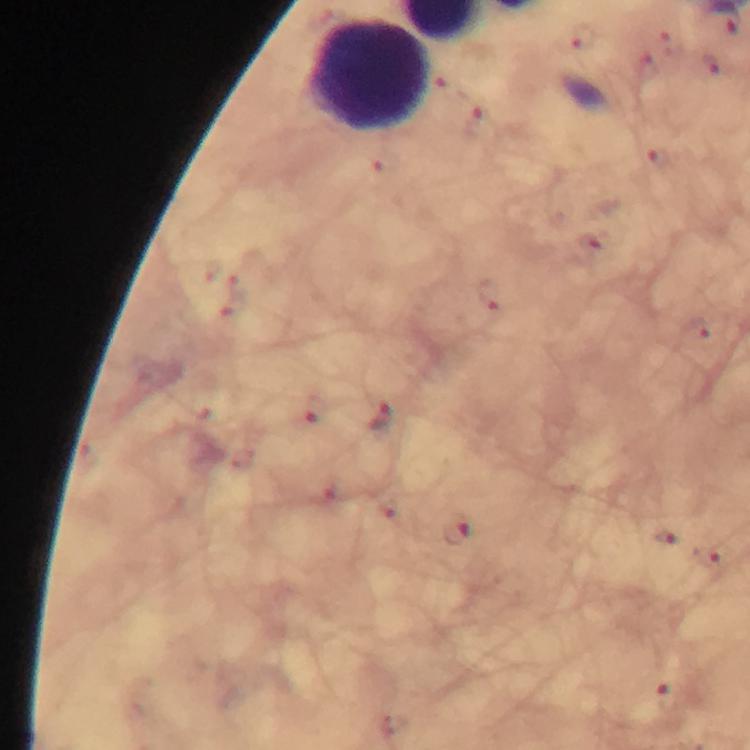

Approximate centers as (x, y) in pixels. Malaria parasite locations: (583, 38), (658, 159), (490, 296), (315, 408), (382, 416), (455, 532), (711, 556). Leukocyte locations: (369, 76). From a diagnostic examination for malaria. Image is 750×750 pixels. Giemsa stain. A crop from one field of view. Thick smear. At 100x magnification. Photographed through the microscope with a smartphone camera. Immersion oil was used.